Assess this cell for malaria.
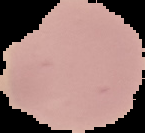
It is uninfected.

Summary:
  - Image type: cell region segmented out of the field of view; surrounding area masked to black
  - Image size: 145×133 pixels
  - Preparation: thin blood smear